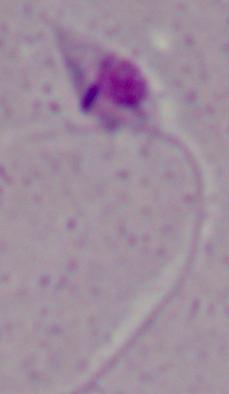 Captured at 1000x magnification. A Leishmania parasite is shown. Micrograph.